Classify this cell by malaria status.
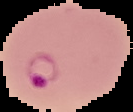

It is parasitized.

image type = segmented cell region with the area outside set to black
preparation = thin blood smear
image size = 133×112 pixels